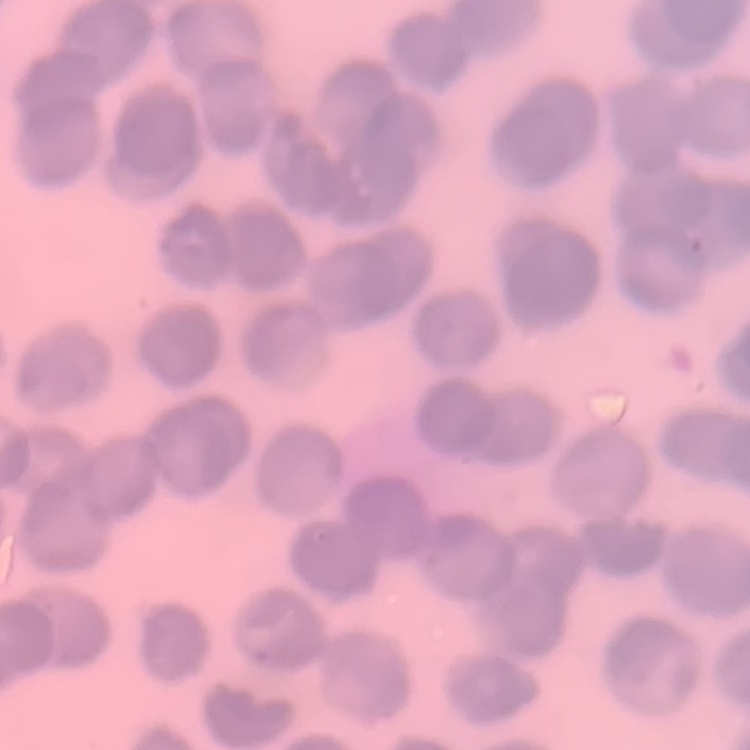

erythrocyte morphology = rouleaux formation
stain = Field's or Giemsa
image type = one tile cut from a larger photomicrograph
preparation = thin blood smear